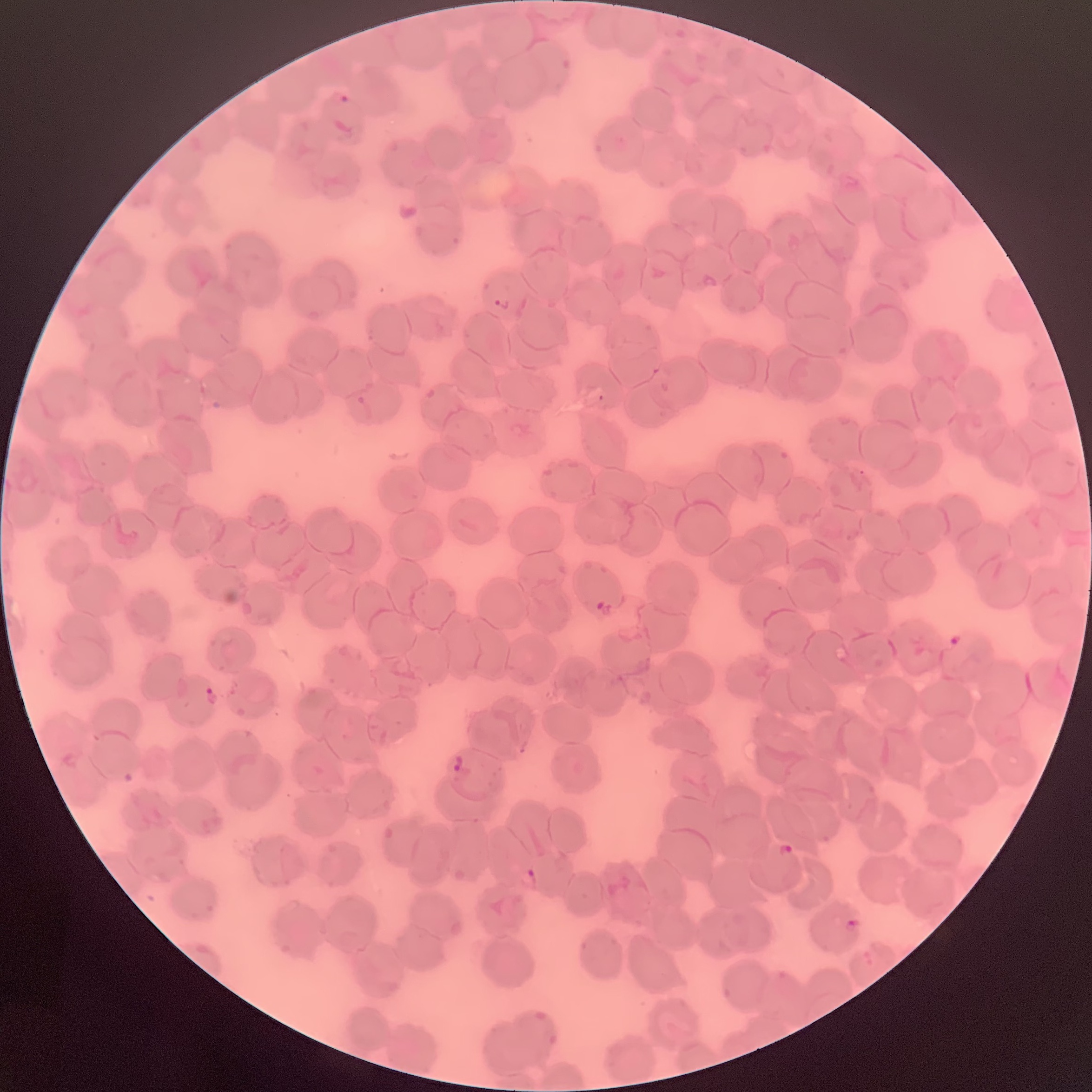

coordinate format = approximate bounding boxes as named x1/y1/x2/y2 corners in pixels
Plasmodium parasite locations = (x1=337, y1=91, x2=350, y2=105), (x1=493, y1=296, x2=510, y2=312), (x1=596, y1=599, x2=606, y2=611), (x1=949, y1=633, x2=962, y2=646), (x1=204, y1=685, x2=218, y2=707), (x1=451, y1=753, x2=464, y2=775), (x1=781, y1=843, x2=795, y2=857), (x1=523, y1=868, x2=539, y2=889), (x1=843, y1=920, x2=859, y2=931)
red blood cell morphology = rouleaux formation
image size = 1092×1092 pixels
preparation = thin blood film
modality = optical microscopy